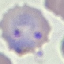
result = malaria parasites detected
preparation = thin blood smear
stain = Giemsa
capture = smartphone through the microscope eyepiece
image type = automatically extracted cell patch, resized to 64 × 64 pixels